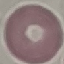
Result: no malaria parasites detected. Automatically extracted cell patch, resized to 64 × 64 pixels. Giemsa-stained preparation. Thin smear of blood. Photographed with a smartphone camera at the microscope eyepiece.